Identify the parasite.
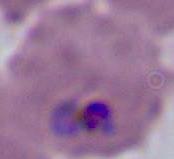

Plasmodium.

Photomicrograph. Captured at either 400x or 1000x magnification.